Classify this cell by malaria status.
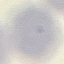
Uninfected.

{
  "stain": "Giemsa",
  "capture": "smartphone camera at the microscope eyepiece",
  "image_type": "automatically extracted cell patch, resized to 64 × 64 pixels",
  "preparation": "thin blood film"
}